Assess the morphology of the erythrocytes.
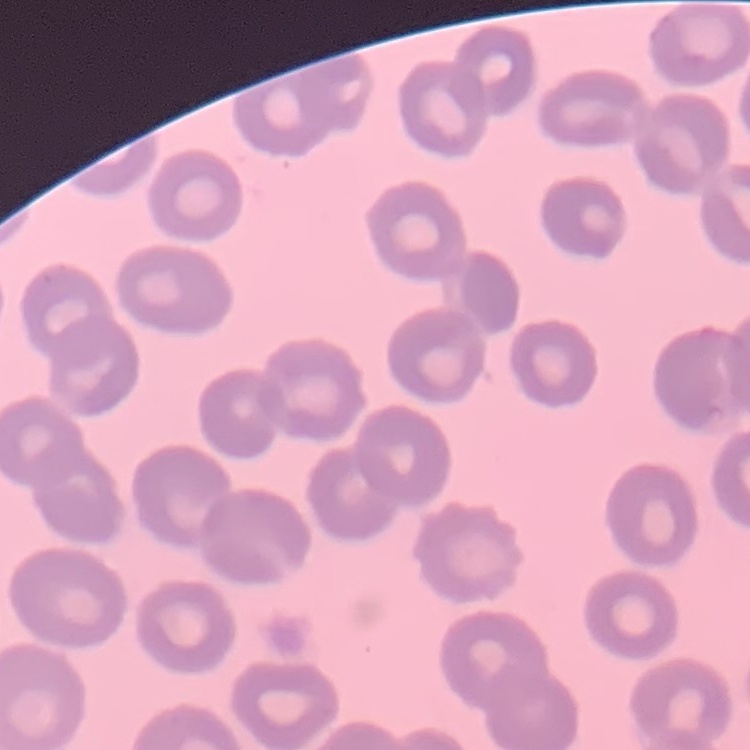

They show no rouleaux formation.

Summary:
  - Stain: Field's or Giemsa
  - Preparation: thin blood film
  - Image type: one tile cut from a larger photomicrograph